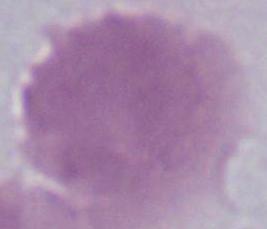

1000x magnification. A red blood cell is shown. Photomicrograph.